Report the malaria status of this cell.
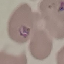

Parasitized.

Summary:
  - Preparation: thin blood smear
  - Capture: smartphone through the microscope eyepiece
  - Image type: automatically extracted cell patch, resized to 64 × 64 pixels
  - Stain: Giemsa